State which parasite is depicted.
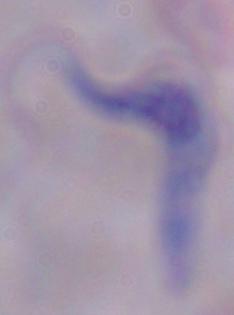

A trypanosome.

Micrograph. Captured at 1000x magnification.